Outline each blood parasite and name the species.
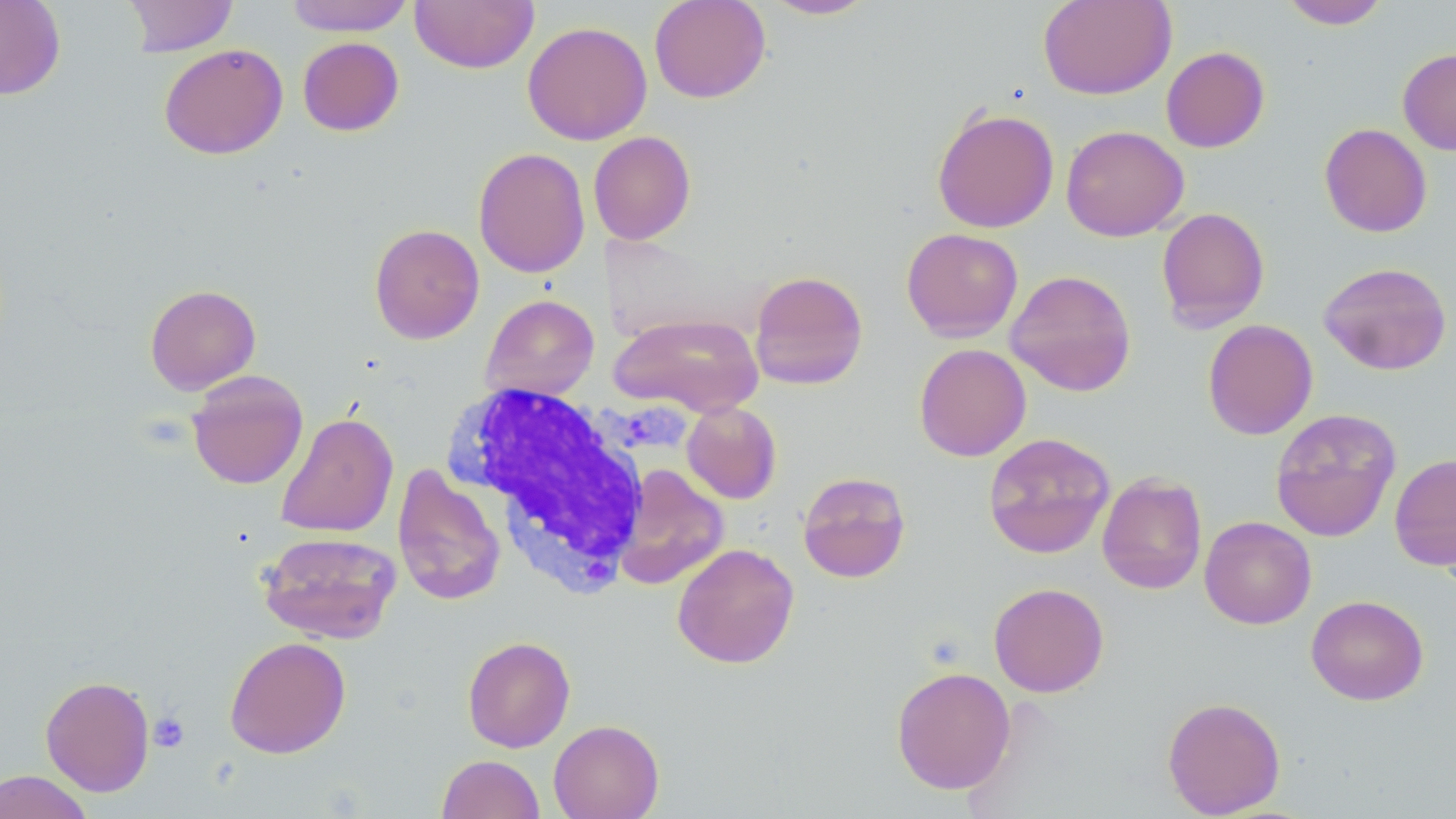
No blood parasites seen.

Approximate bounding boxes as (x1, y1, x2, y2) in pixels. Uninfected red blood cell locations: (0, 0, 66, 100), (123, 0, 238, 57), (284, 0, 414, 36), (410, 0, 538, 73), (648, 0, 771, 103), (760, 0, 880, 20), (1038, 0, 1176, 99), (1279, 0, 1391, 29), (522, 21, 652, 145), (297, 36, 404, 136), (159, 43, 288, 160), (1161, 46, 1270, 153), (1398, 49, 1456, 155), (932, 107, 1059, 234), (1318, 123, 1432, 237), (1060, 125, 1189, 241), (588, 131, 696, 245), (473, 147, 591, 278), (1156, 207, 1270, 332), (369, 223, 485, 344), (901, 228, 1023, 342), (1318, 261, 1452, 375), (1005, 269, 1137, 396), (749, 270, 868, 390), (145, 284, 261, 395), (481, 294, 599, 401), (610, 312, 764, 417), (1202, 319, 1318, 440), (914, 343, 1031, 461), (187, 371, 308, 489), (681, 401, 782, 504), (1270, 407, 1401, 543), (276, 411, 399, 538), (983, 432, 1116, 559), (1389, 452, 1456, 572), (392, 463, 506, 606), (613, 465, 729, 590), (797, 471, 911, 583), (1096, 472, 1207, 594), (1199, 516, 1316, 629), (258, 531, 402, 644), (672, 543, 799, 669), (988, 582, 1109, 697), (1306, 594, 1429, 706), (462, 635, 575, 752), (224, 636, 351, 759), (891, 666, 1016, 794), (40, 675, 156, 796), (1162, 696, 1286, 817), (548, 719, 665, 819), (436, 754, 545, 819), (0, 769, 93, 819). White blood cell locations: (445, 384, 652, 594). Platelet locations: (149, 712, 189, 752). Slide-level diagnosis: negative for blood parasites. Image is 1456×819 pixels. Thin blood film. May-Grünwald-Giemsa-stained preparation. Single field of view. Captured at 1000x magnification. Light microscopy.